Identify the parasite.
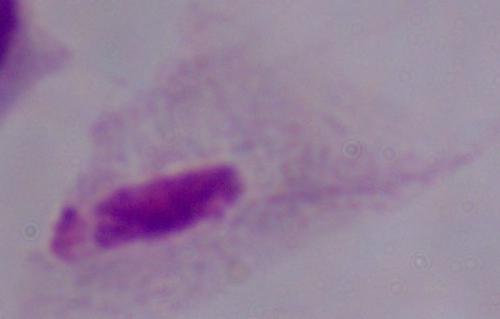
A trichomonad.

modality = photomicrograph
magnification = 1000x